Describe the morphology of the red blood cells.
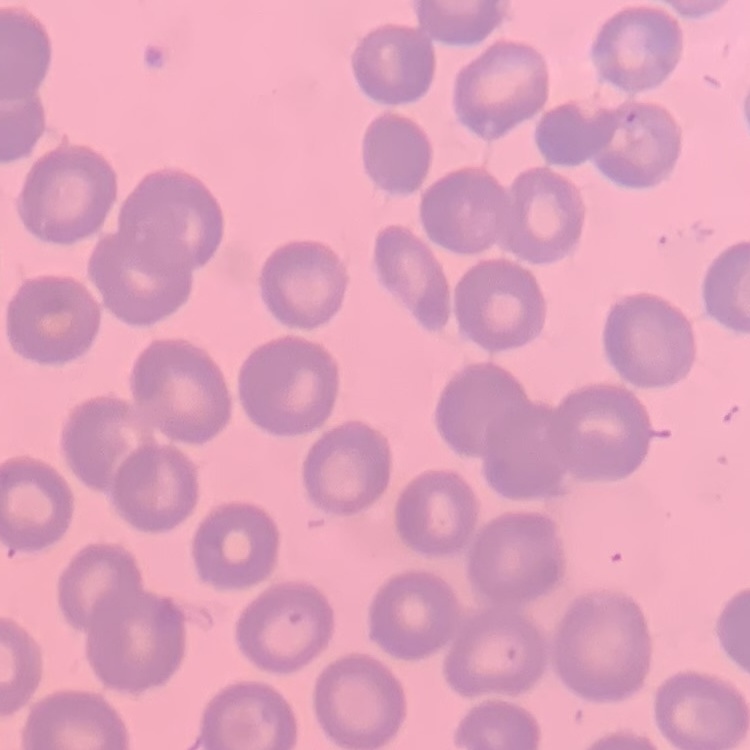
No rouleaux formation.

One tile cut from a larger photomicrograph. Thin blood film. Field's or Giemsa stain.